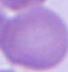
Summary:
  - Modality: photomicrograph
  - Magnification: 1000x
  - Identification: red blood cell